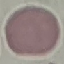
result = negative for malaria parasites
capture = smartphone through the microscope eyepiece
stain = Giemsa
preparation = thin blood smear
image type = cell patch, automatically extracted from a larger field of view and resized to 64 × 64 pixels